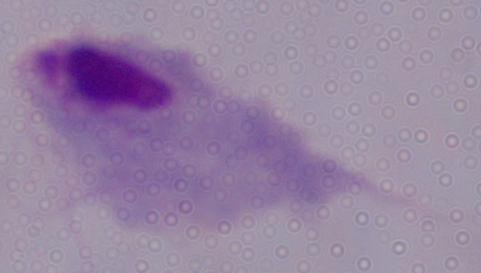

magnification: 1000x
identification: trichomonad
modality: photomicrograph